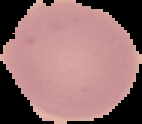

{
  "malaria_status": "uninfected",
  "image_type": "cell region segmented out of the field of view; surrounding area masked to black",
  "image_size": "142×124 pixels",
  "preparation": "thin blood film"
}